Assess the morphology of the red blood cells.
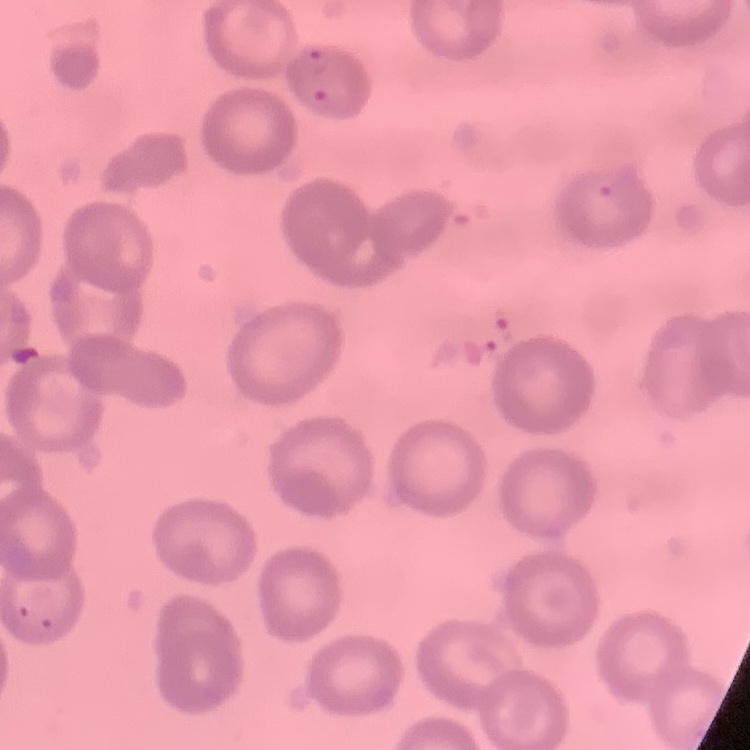

No rouleaux formation.

Field's or Giemsa stain. Square crop of a larger photomicrograph. Thin blood smear.